Describe the morphology of the red blood cells.
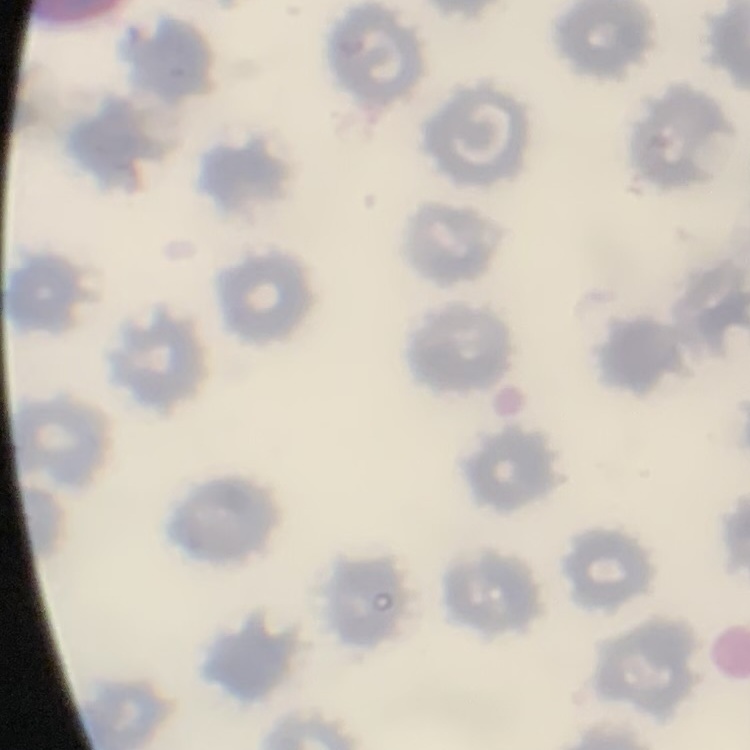
They show no rouleaux formation.

Summary:
  - Preparation: thin blood film
  - Image type: one tile cut from a larger photomicrograph
  - Stain: Field's or Giemsa